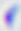

Summary:
  - Identification: Toxoplasma gondii
  - Magnification: 400x
  - Modality: photomicrograph